Identify the blood parasite species.
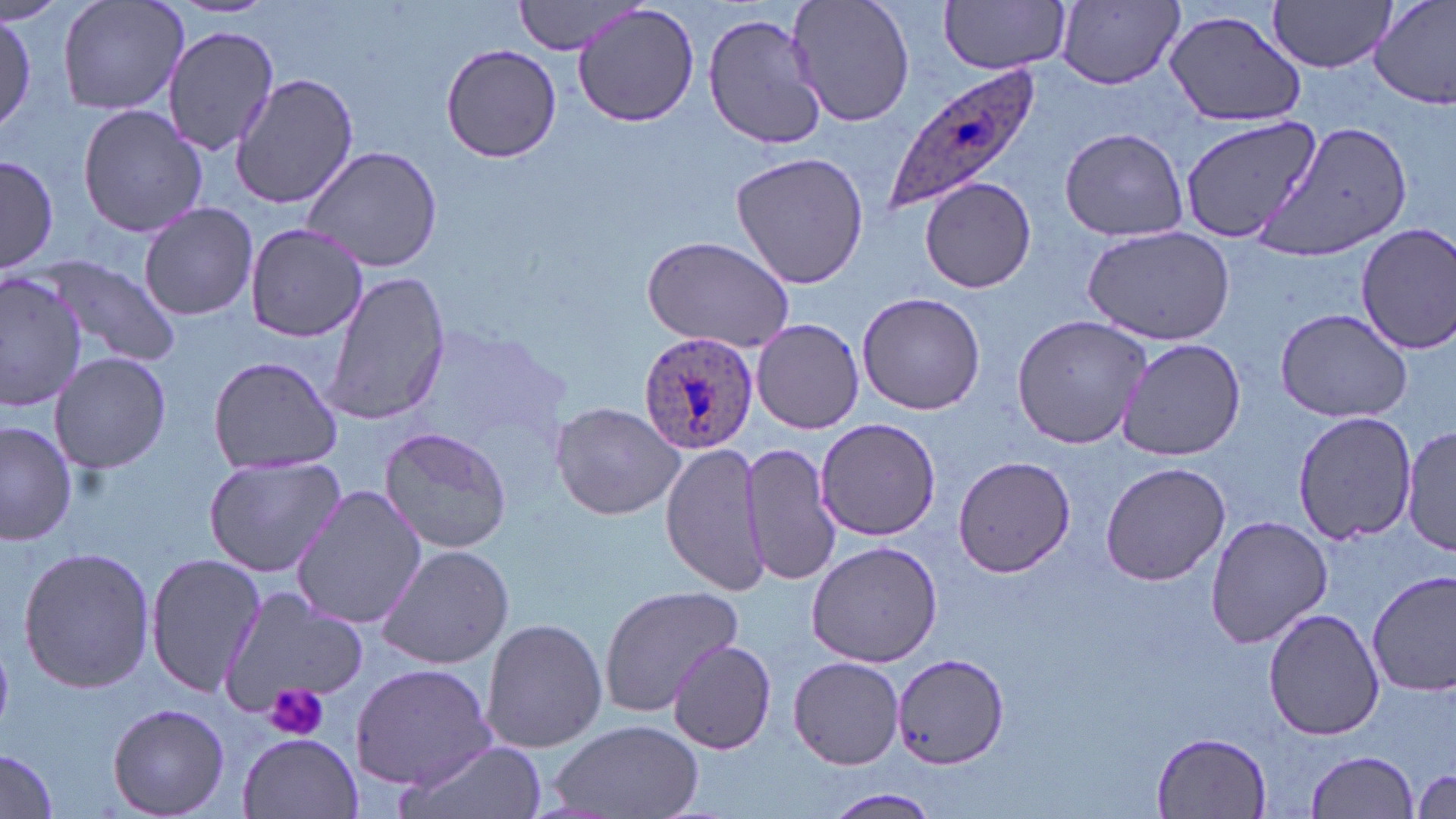
Plasmodium ovale.

modality = optical microscopy
magnification = 1000x
Plasmodium ovale-infected red blood cell locations = approximate bounding boxes as (x1,y1)-(x2,y2) corner pairs in pixels: (877,68)-(1040,216), (639,332)-(761,456)
preparation = thin blood smear
uninfected red blood cell locations = approximate bounding boxes as (x1,y1)-(x2,y2) corner pairs in pixels: (57,0)-(188,116), (511,0)-(647,55), (787,0)-(916,128), (939,0)-(1071,75), (1268,0)-(1396,72), (1370,0)-(1456,110), (574,2)-(700,129), (1056,2)-(1185,89), (1163,10)-(1307,128), (0,11)-(36,137), (703,13)-(825,150), (162,23)-(280,155), (440,42)-(562,165), (231,73)-(361,211), (77,101)-(206,238), (1180,115)-(1322,249), (1254,120)-(1412,261), (1058,126)-(1188,241), (299,144)-(445,276), (729,150)-(871,291), (1,154)-(58,275), (921,177)-(1035,293), (137,202)-(259,320), (243,222)-(369,343), (1354,222)-(1456,355), (1083,226)-(1237,348), (641,234)-(797,353), (36,254)-(183,368), (1,268)-(85,411), (320,270)-(448,428), (856,291)-(987,416), (1272,306)-(1416,424), (1010,314)-(1152,451), (751,317)-(865,434), (1116,337)-(1247,462), (50,349)-(171,474), (207,355)-(344,474), (550,400)-(687,521), (1291,409)-(1418,544), (813,418)-(941,541), (0,420)-(77,549), (1402,424)-(1456,557), (378,425)-(515,553), (660,441)-(772,599), (738,441)-(842,586), (202,454)-(346,576), (952,456)-(1075,577), (1099,460)-(1230,586), (289,483)-(426,632), (1204,516)-(1332,649), (806,539)-(943,668), (372,540)-(515,670), (15,546)-(156,694), (144,553)-(265,699), (1367,570)-(1456,700), (598,585)-(743,717), (218,590)-(367,719), (1262,606)-(1384,740), (479,616)-(609,754), (666,640)-(777,755), (891,651)-(1009,771), (789,655)-(905,770), (351,663)-(494,790), (108,702)-(230,817), (546,718)-(705,819), (1151,731)-(1271,816), (237,732)-(361,818), (391,739)-(548,819), (0,749)-(61,818), (1305,751)-(1419,818), (1413,767)-(1455,815), (827,790)-(939,817)
stain = May-Grünwald-Giemsa
platelet locations = approximate bounding boxes as (x1,y1)-(x2,y2) corner pairs in pixels: (263,683)-(330,741)
field of view = one of a larger specimen
image size = 1456×819 pixels